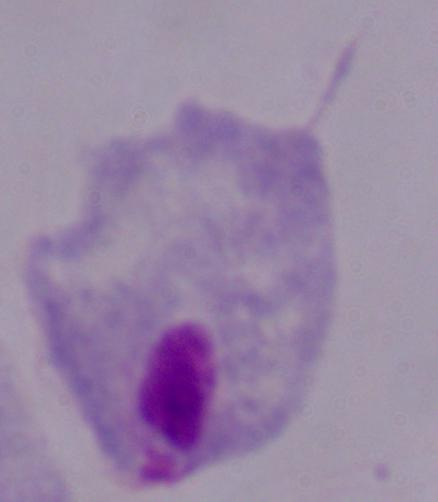

Summary:
  - Magnification: 1000x
  - Identification: trichomonad
  - Modality: micrograph